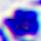
A white blood cell is seen. Photomicrograph. 400x magnification.